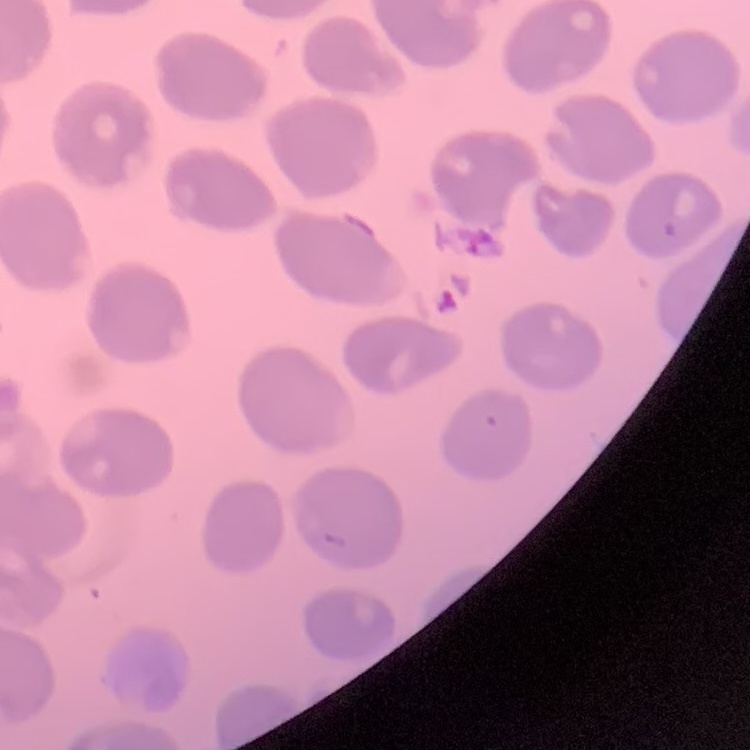
red blood cell morphology = no rouleaux formation
preparation = thin peripheral smear
image type = one tile cut from a larger photomicrograph
stain = Field's or Giemsa